Classify this cell by malaria status.
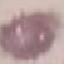

It is uninfected.

Thin blood film. Giemsa stain. Acquired by smartphone through the microscope eyepiece. Automatically extracted cell patch, resized to 64 × 64 pixels.